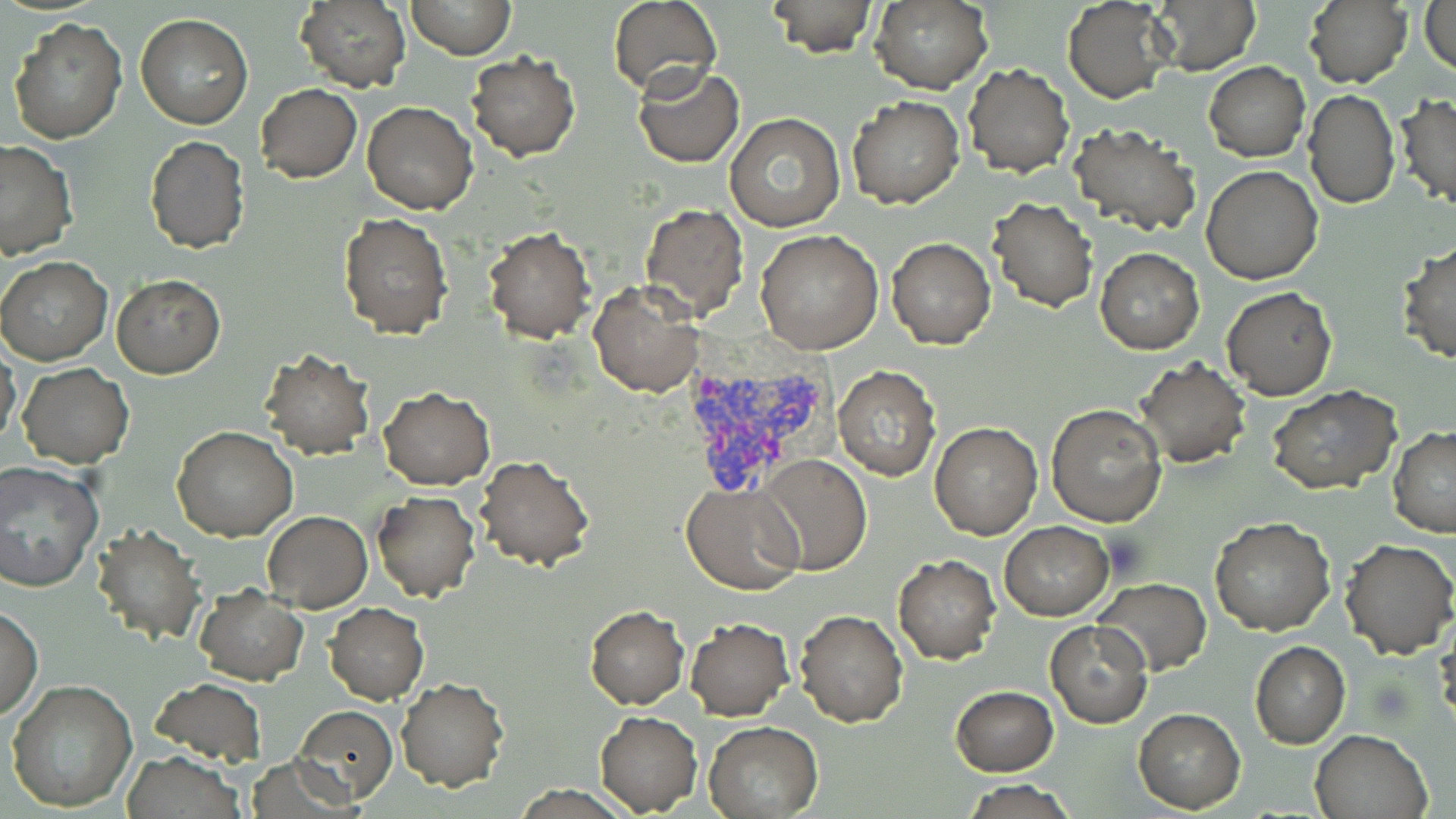
Summary:
  - Coordinate format: approximate bounding boxes as [x1, y1, x2, y2] in pixels
  - Uninfected red blood cell locations: [293, 0, 411, 91], [405, 0, 515, 60], [765, 0, 877, 56], [1303, 0, 1413, 91], [608, 1, 723, 96], [870, 1, 992, 93], [1062, 1, 1174, 104], [1152, 1, 1257, 73], [1421, 1, 1455, 78], [136, 13, 252, 128], [6, 16, 128, 143], [467, 50, 580, 162], [1203, 61, 1310, 162], [964, 63, 1075, 178], [632, 65, 744, 166], [256, 83, 363, 183], [1305, 90, 1400, 208], [846, 95, 964, 208], [1395, 95, 1456, 209], [361, 101, 477, 214], [725, 112, 845, 232], [1069, 122, 1202, 237], [145, 135, 250, 254], [0, 139, 76, 260], [1202, 165, 1323, 284], [987, 197, 1097, 312], [639, 202, 749, 319], [337, 212, 452, 338], [483, 227, 596, 344], [756, 230, 885, 355], [888, 238, 995, 349], [1396, 241, 1456, 365], [1095, 247, 1204, 354], [0, 256, 114, 365], [112, 276, 226, 378], [589, 282, 702, 397], [1222, 285, 1338, 401], [0, 345, 23, 447], [260, 350, 374, 460], [1136, 358, 1250, 469], [18, 362, 134, 467], [832, 366, 939, 480], [1268, 385, 1401, 495], [378, 388, 494, 490], [1045, 403, 1168, 527], [929, 422, 1043, 539], [173, 426, 297, 541], [1388, 427, 1456, 538], [476, 454, 595, 572], [758, 455, 871, 575], [0, 461, 102, 593], [681, 482, 806, 594], [372, 491, 481, 603], [262, 510, 373, 612], [1209, 516, 1336, 636], [1000, 521, 1113, 620], [94, 524, 205, 644], [1338, 538, 1455, 657], [894, 554, 1001, 664], [1094, 577, 1211, 675], [194, 585, 307, 683], [325, 602, 428, 704], [1, 606, 43, 720], [584, 606, 690, 710], [793, 610, 909, 729], [684, 619, 794, 720], [1044, 620, 1152, 728], [1249, 642, 1350, 749], [152, 676, 267, 767], [395, 678, 509, 791], [6, 679, 137, 813], [951, 686, 1059, 776], [294, 705, 398, 804], [1134, 709, 1245, 812], [594, 711, 703, 815], [703, 721, 823, 817], [1309, 729, 1432, 819], [120, 751, 245, 818], [961, 779, 1079, 818]
  - Plasmodium vivax-infected red blood cell locations: [679, 362, 833, 497]
  - Slide-level diagnosis: Plasmodium vivax
  - Image size: 1456×819 pixels
  - Field of view: single
  - Modality: optical microscopy
  - Stain: May-Grünwald-Giemsa
  - Preparation: thin blood film
  - Magnification: 1000x